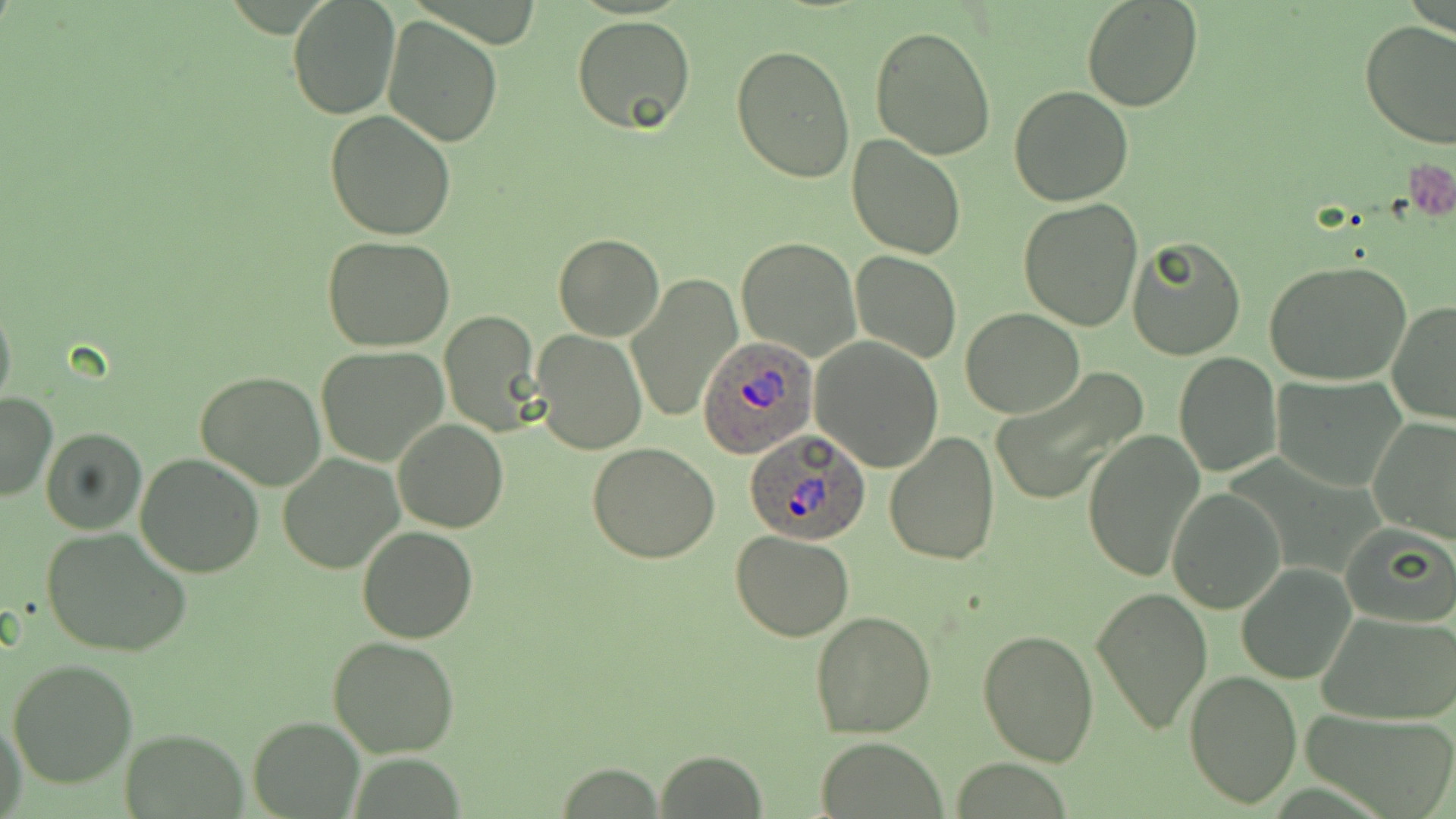
slide-level diagnosis = Plasmodium ovale
preparation = thin blood smear
Plasmodium ovale-infected red blood cell locations = approximate bounding boxes as (x1, y1, x2, y2) in pixels: (695, 336, 818, 460), (744, 431, 873, 545)
stain = May-Grünwald-Giemsa
image size = 1456×819 pixels
platelet locations = approximate bounding boxes as (x1, y1, x2, y2) in pixels: (1406, 157, 1454, 219)
uninfected red blood cell locations = approximate bounding boxes as (x1, y1, x2, y2) in pixels: (287, 0, 401, 121), (1082, 0, 1203, 112), (382, 14, 503, 149), (571, 15, 697, 135), (1359, 19, 1456, 149), (869, 24, 998, 160), (731, 41, 856, 184), (1010, 85, 1133, 205), (324, 112, 457, 243), (846, 135, 965, 260), (1018, 198, 1144, 333), (553, 234, 665, 341), (322, 235, 457, 351), (736, 237, 861, 360), (1127, 237, 1246, 361), (849, 250, 961, 365), (1265, 260, 1412, 388), (626, 273, 742, 424), (0, 294, 16, 416), (1386, 299, 1456, 426), (960, 308, 1085, 419), (439, 310, 543, 436), (532, 330, 646, 456), (811, 335, 945, 471), (317, 344, 449, 467), (1173, 352, 1281, 476), (994, 366, 1148, 509), (195, 371, 327, 491), (1270, 376, 1406, 491), (0, 392, 57, 504), (1367, 415, 1455, 544), (393, 418, 508, 532), (40, 427, 146, 535), (1081, 430, 1204, 584), (884, 433, 1001, 566), (587, 442, 720, 564), (135, 452, 266, 577), (278, 453, 402, 574), (1167, 489, 1285, 614), (1338, 519, 1454, 626), (41, 525, 194, 661), (357, 526, 478, 643), (731, 530, 855, 641), (1236, 564, 1357, 685), (1089, 585, 1213, 735), (808, 609, 937, 738), (1319, 612, 1456, 725), (976, 629, 1100, 766), (327, 633, 460, 758), (7, 659, 137, 788), (1185, 670, 1303, 810), (1300, 707, 1456, 819), (1, 715, 27, 819), (246, 716, 363, 818), (119, 731, 249, 815), (813, 737, 949, 819), (652, 752, 767, 818), (550, 765, 667, 815)
magnification = 1000x
modality = light microscopy
field of view = one of a larger specimen